Report the malaria status of this cell.
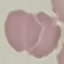

Uninfected.

Acquired by smartphone through the microscope eyepiece. Thin blood film. Cell patch, automatically extracted from a larger field of view and resized to 64 × 64 pixels. Giemsa stain.